Assess for parasitized red blood cells.
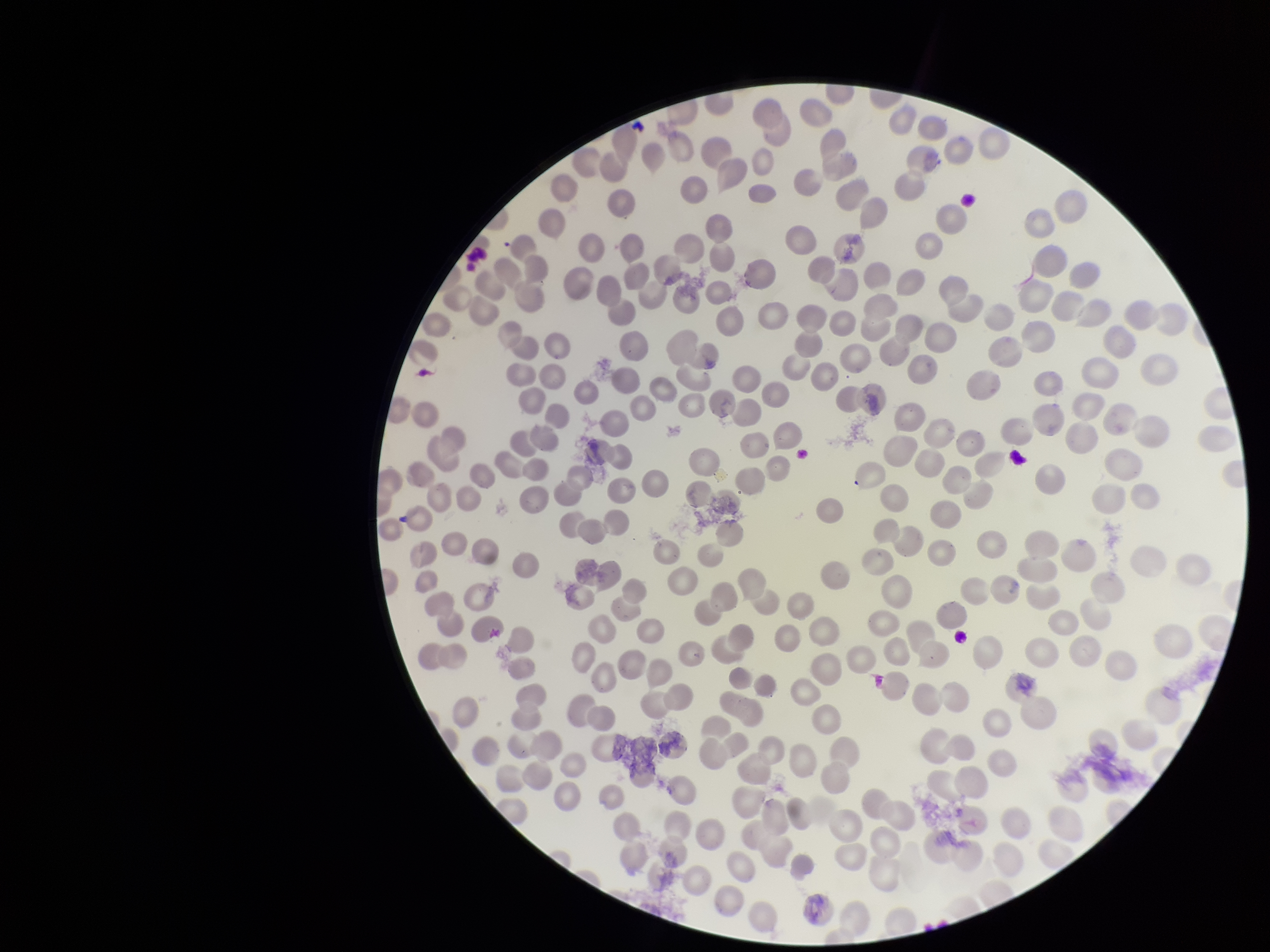

None seen.

Preparation: thin blood smear. Smartphone photograph taken through the eyepiece of a microscope. Patient malaria status: negative. Giemsa stain. One field from this slide. Image is 1270×952 pixels. Red blood cell count: 248. Parasitized red blood cell count: 0.